Give the extent of all uninfected red blood cells.
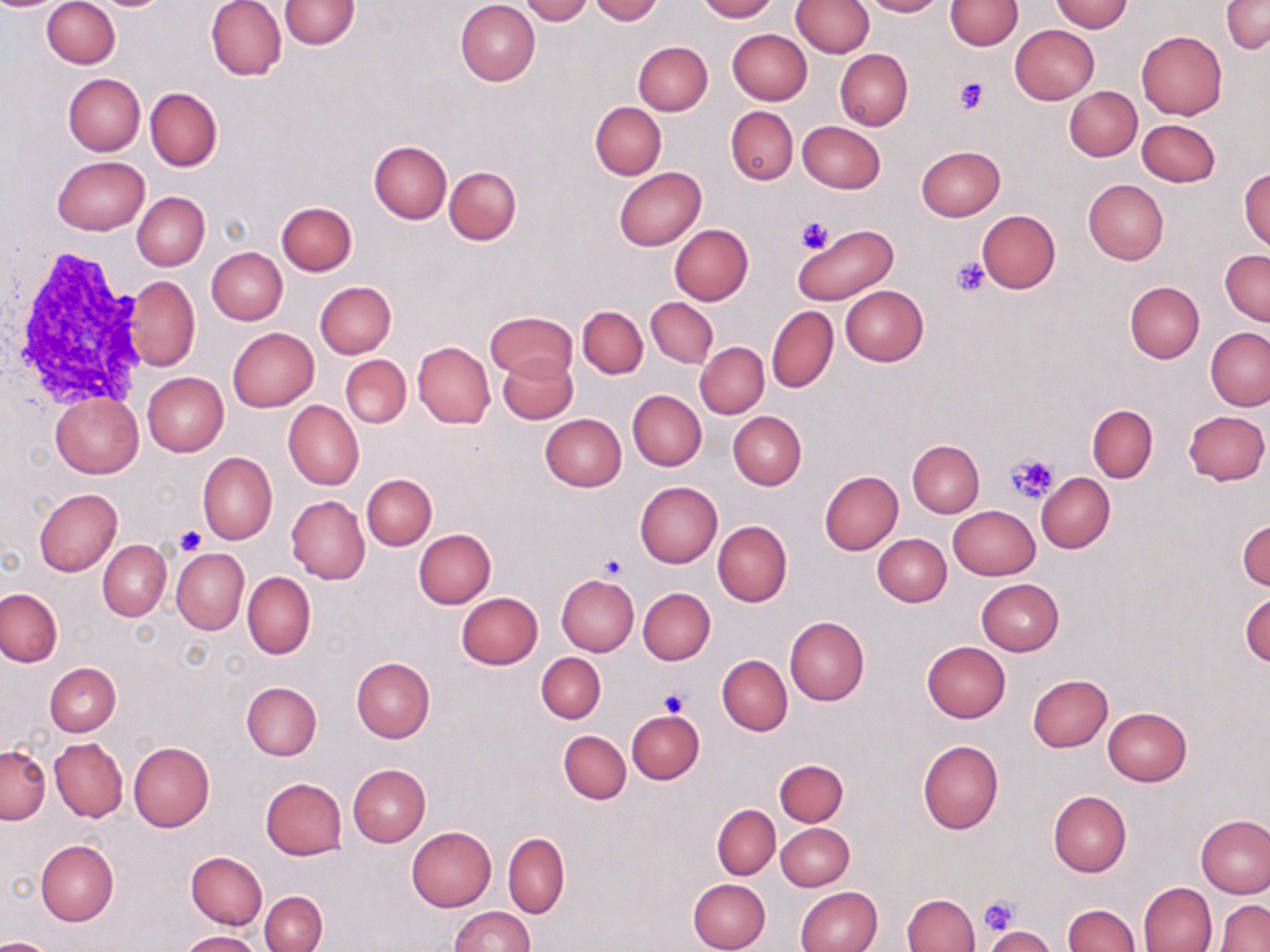
Approximate bounding boxes as (x1,y1)-(x2,y2) corner pairs in pixels.
Uninfected red blood cells: (42,0)-(120,69), (206,0)-(287,81), (280,0)-(360,49), (521,0)-(592,24), (589,0)-(662,24), (696,0)-(775,21), (792,0)-(873,58), (861,0)-(944,17), (944,0)-(1021,51), (1222,0)-(1269,53), (455,1)-(540,86), (1051,1)-(1133,32), (1010,25)-(1098,104), (727,29)-(811,105), (1136,30)-(1227,119), (633,41)-(712,115), (835,50)-(912,130), (63,73)-(145,155), (145,87)-(223,173), (1064,87)-(1141,161), (590,101)-(666,180), (725,107)-(798,185), (1137,119)-(1220,187), (798,121)-(885,193), (369,142)-(451,223), (915,145)-(1006,221), (52,155)-(150,236), (444,165)-(522,246), (614,167)-(706,250), (1239,167)-(1269,253), (1083,179)-(1169,264), (132,192)-(209,271), (276,201)-(357,276), (977,210)-(1060,292), (792,224)-(897,306), (669,225)-(753,305), (206,247)-(287,325), (1221,249)-(1269,325), (123,275)-(199,371), (315,281)-(395,359), (1124,281)-(1203,362), (840,285)-(929,366), (646,296)-(717,368), (577,306)-(648,379), (766,306)-(838,393), (485,312)-(576,382), (227,328)-(319,412), (1205,328)-(1270,410), (413,341)-(495,428), (696,343)-(768,418), (498,354)-(578,423), (341,355)-(411,428), (143,373)-(228,455), (628,390)-(706,470), (51,394)-(144,478), (283,401)-(363,491), (1087,403)-(1157,482), (1183,410)-(1269,485), (728,411)-(806,490), (540,414)-(626,492), (908,440)-(984,518), (198,452)-(276,545), (819,471)-(903,554), (1036,473)-(1115,553), (362,474)-(437,550), (634,481)-(723,567), (34,488)-(123,576), (286,495)-(369,585), (948,506)-(1040,580), (1238,516)-(1269,592), (712,521)-(792,607), (414,529)-(495,608), (872,534)-(951,606), (98,539)-(170,621), (171,549)-(248,635), (242,572)-(316,659), (556,574)-(639,656), (976,578)-(1064,656), (0,588)-(63,667), (638,588)-(715,664), (1242,590)-(1270,669), (456,592)-(543,669), (785,617)-(869,705), (922,641)-(1011,722), (536,653)-(606,723), (717,655)-(793,735), (351,657)-(435,742), (45,663)-(121,735), (1026,674)-(1112,752), (241,681)-(322,760), (1102,708)-(1191,786), (627,709)-(704,784), (559,730)-(630,804), (49,738)-(127,822), (917,740)-(1003,834), (128,743)-(214,832), (0,745)-(50,824), (775,759)-(849,826), (348,764)-(431,846), (260,778)-(348,860), (1048,790)-(1132,876), (712,805)-(780,880), (1196,815)-(1270,897), (776,823)-(853,890), (407,826)-(496,910), (504,833)-(569,918), (35,841)-(118,926), (186,851)-(266,930), (688,879)-(770,952), (1139,882)-(1216,951), (796,887)-(883,952), (260,892)-(326,952), (902,893)-(980,951), (1214,900)-(1270,952), (1064,905)-(1140,952), (448,906)-(534,952), (984,926)-(1055,952), (179,931)-(261,951), (0,937)-(56,952).

Platelet locations: (954,76)-(988,114), (795,217)-(831,255), (951,256)-(992,297), (1007,451)-(1059,504), (175,525)-(208,557), (600,555)-(627,580), (657,689)-(689,716), (979,896)-(1020,936). White blood cell locations: (9,254)-(146,407). Slide-level diagnosis: no evidence of blood parasites. Image is 1270×952 pixels. May-Grünwald-Giemsa stain. Single field of view. Captured at 1000x magnification. Optical microscopy. Thin blood smear.